Point out each leukocyte.
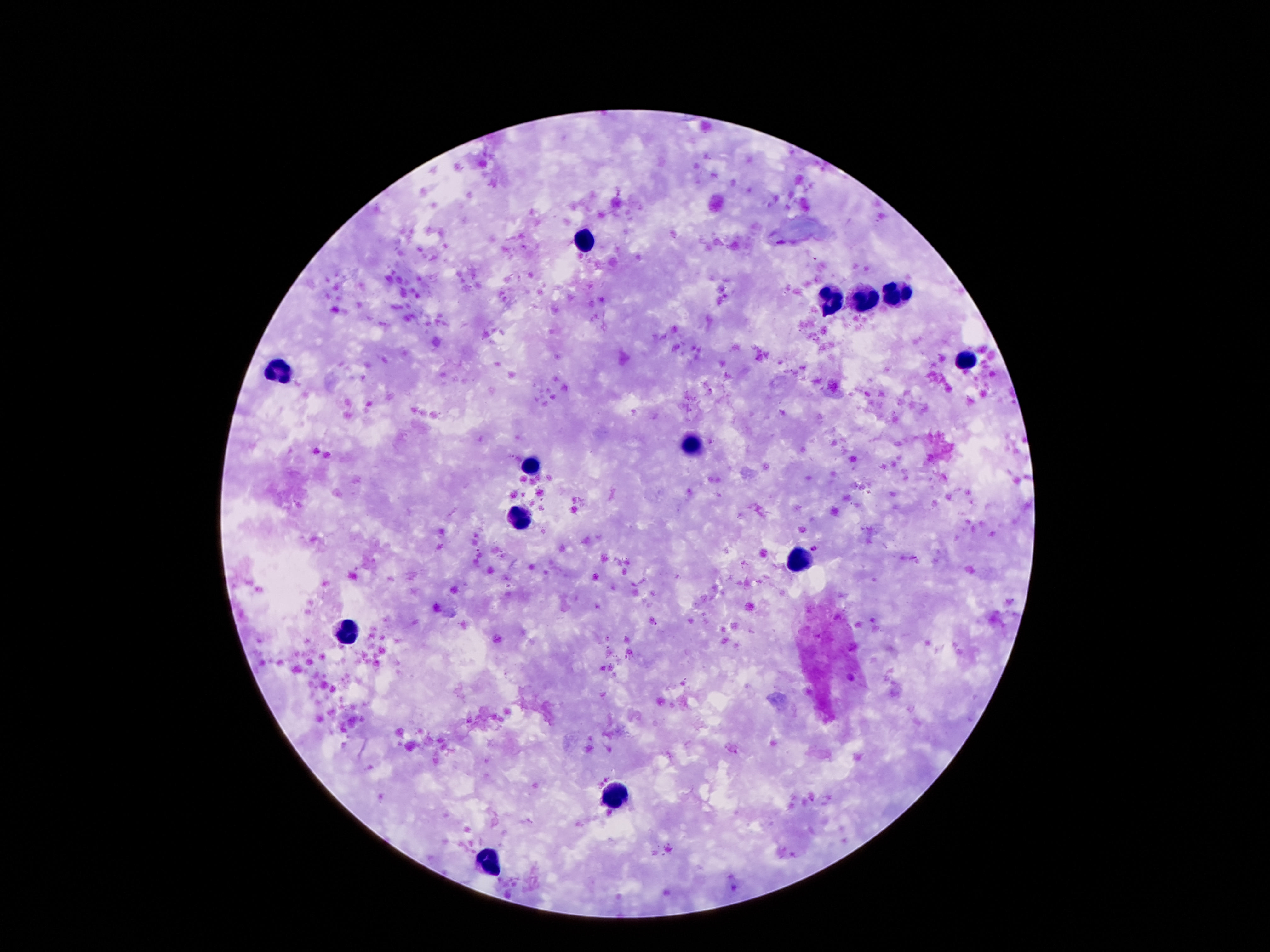

Approximate object centers, in pixels from the top-left corner.
Leukocytes: (x=580, y=237), (x=898, y=289), (x=832, y=301), (x=865, y=301), (x=969, y=359), (x=284, y=373), (x=692, y=444), (x=533, y=466), (x=520, y=521), (x=800, y=560), (x=347, y=632), (x=610, y=798), (x=491, y=861).

Summary:
  - Patient malaria status: not infected
  - Magnification: 100x
  - Field of view: single
  - Image size: 1270×952 pixels
  - Preparation: thick blood smear
  - Capture: smartphone camera through the microscope eyepiece
  - Stain: Giemsa